Classify this cell by malaria status.
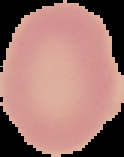

Uninfected.

preparation = thin blood film
image size = 124×157 pixels
image type = segmented cell region on a black background